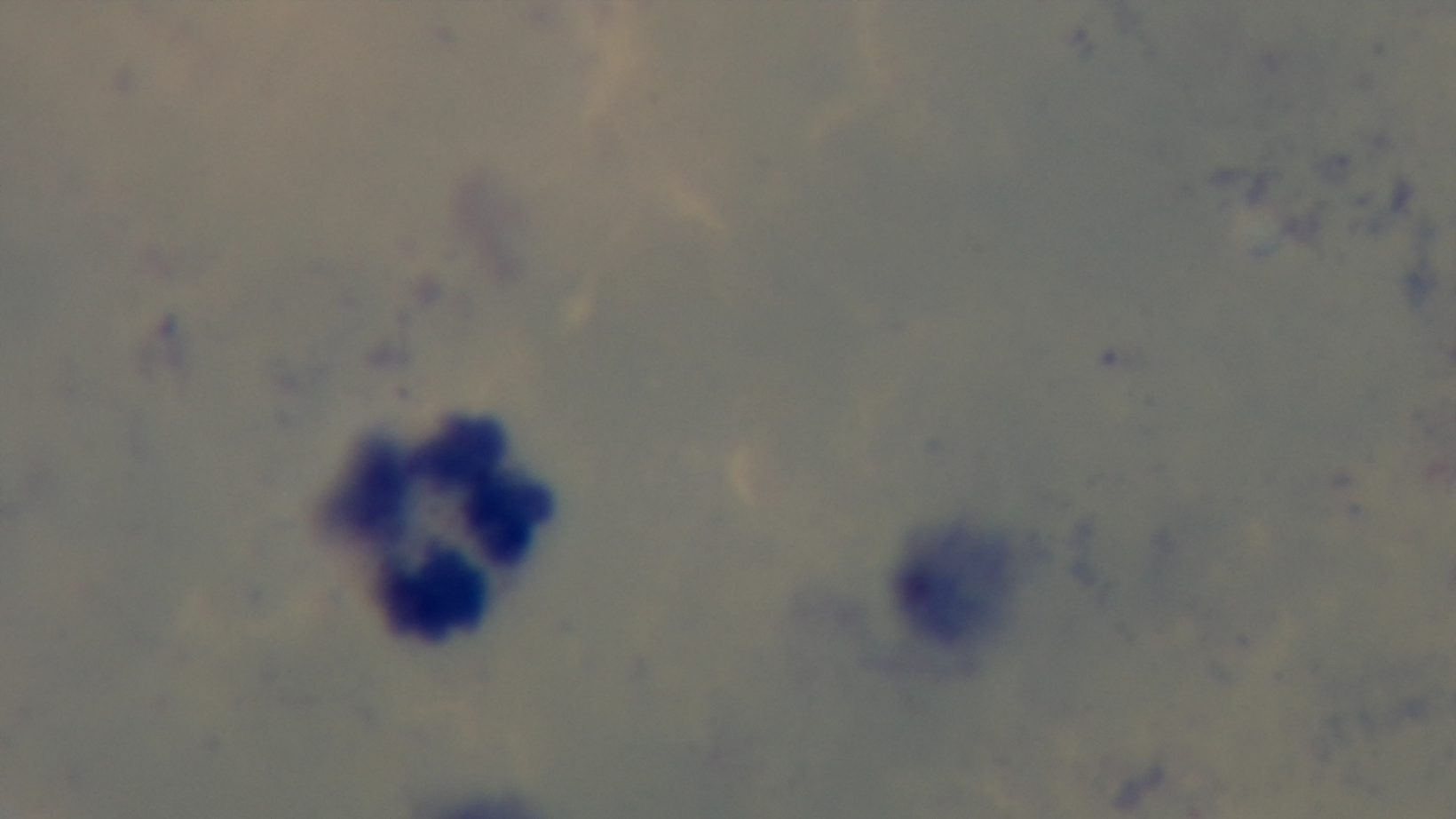
objective = 100x oil immersion
modality = light microscopy
capture = mounted 4K digital camera
malaria status = negative
preparation = thick blood film
field of view = one from the slide
stain = Giemsa